Point out each malaria parasite.
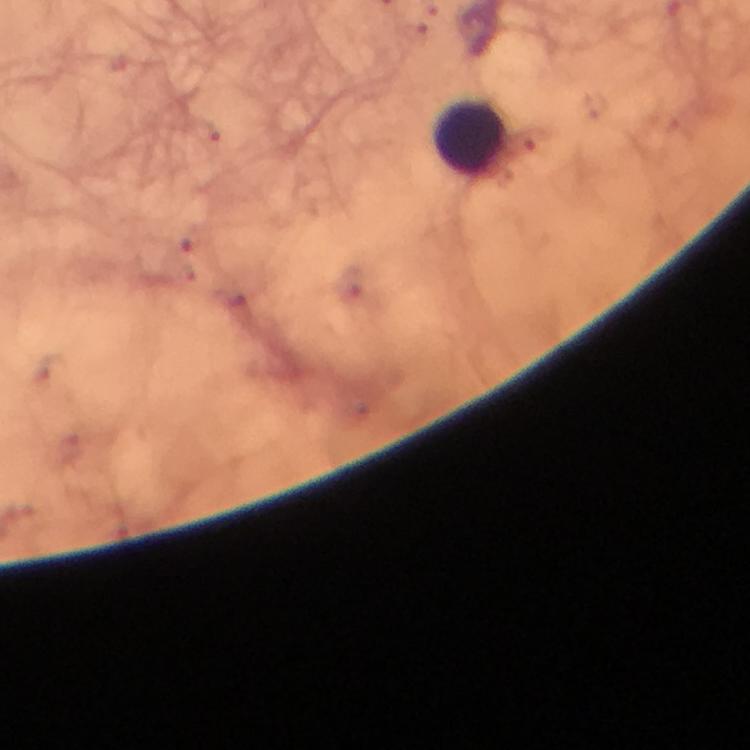

No malaria parasites seen.

Approximate centers as {x, y} in pixels.
Summary:
  - Leukocyte locations: {472, 137}
  - Image size: 750×750 pixels
  - Stain: Giemsa
  - Cropped from: one field of view
  - Context: from a malaria diagnostic workup
  - Immersion oil: used
  - Magnification: 100x
  - Capture: smartphone photograph through a microscope
  - Preparation: thick blood smear